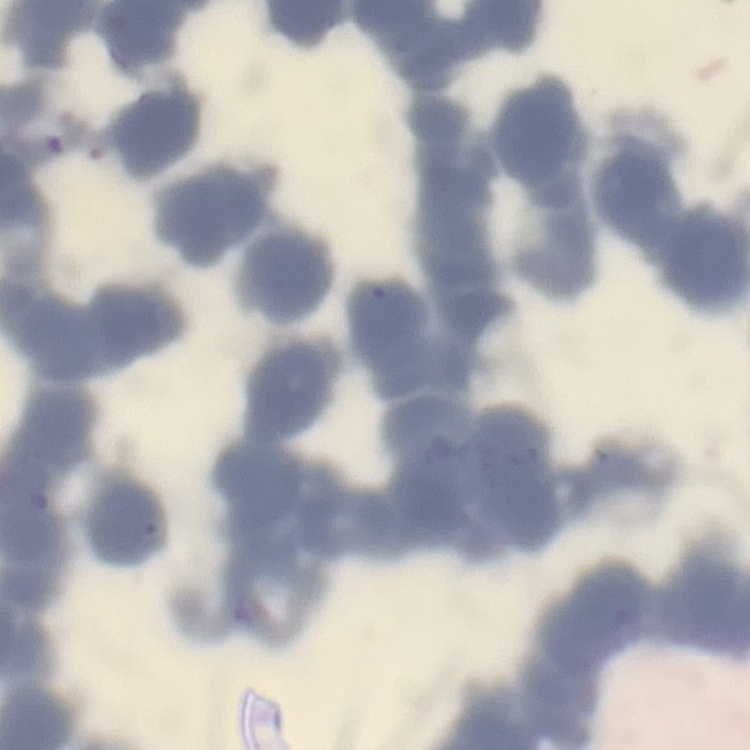

The erythrocytes show rouleaux formation. Field's or Giemsa stain. One tile cut from a larger photomicrograph. Thin peripheral smear.